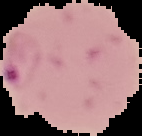
Summary:
  - Image type: segmented cell region with the area outside set to black
  - Result: Plasmodium parasites identified
  - Image size: 142×136 pixels
  - Preparation: thin blood smear